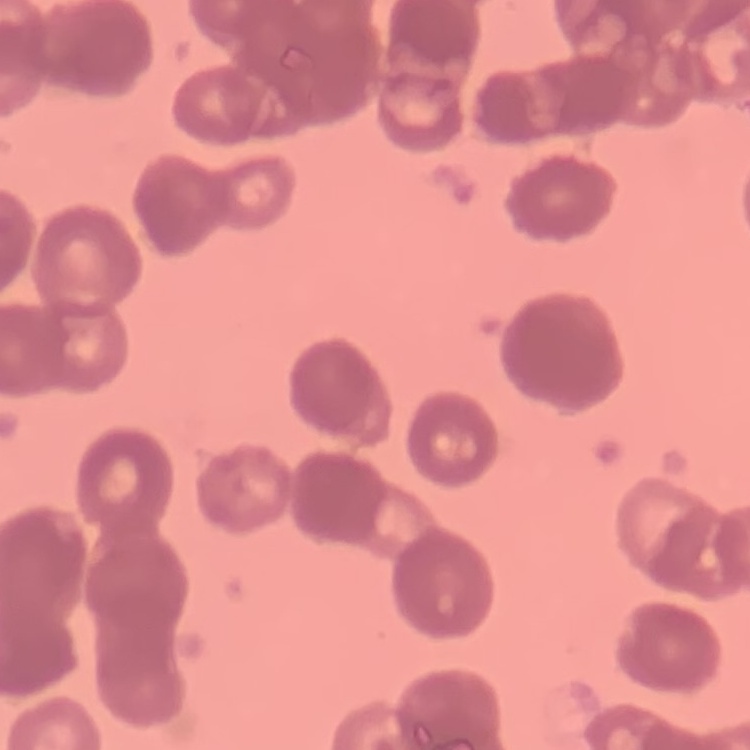

The erythrocytes show rouleaux formation. Field's or Giemsa stain. One tile cut from a larger photomicrograph. Thin blood smear.